Point out each Plasmodium parasite.
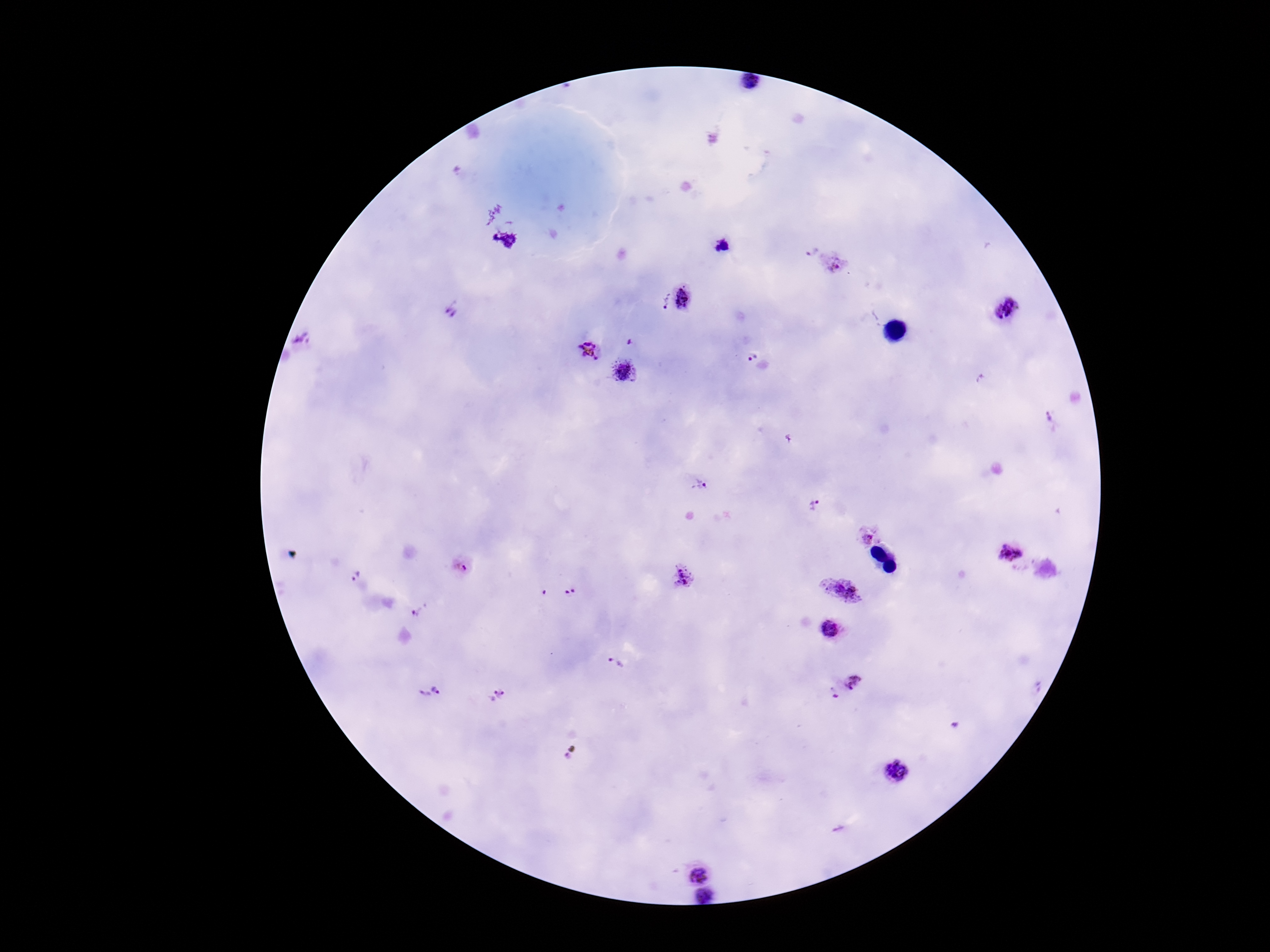
Approximate centers as (x, y) in pixels.
Plasmodium parasites: (722, 246), (809, 249), (835, 265), (684, 299), (661, 303), (1005, 310), (451, 314), (299, 340), (630, 342), (590, 351), (752, 356), (623, 371), (1050, 419), (699, 483), (813, 505), (867, 536), (1009, 554), (462, 567), (353, 576), (684, 578), (841, 591), (571, 592), (544, 593), (419, 611), (832, 631), (617, 663), (855, 681), (440, 686), (834, 694), (420, 695), (498, 695), (896, 773), (697, 867), (705, 898).

Photographed through the microscope eyepiece with a smartphone camera. Image is 1270×952 pixels. Thick blood film. Patient malaria status: positive. Giemsa stain. One field from this slide. 100x magnification.